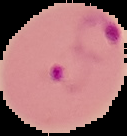

From a thin blood smear. Malaria status: parasitized. Image is 127×136 pixels. Segmented cell region on a black background.